Locate every uninfected red blood cell.
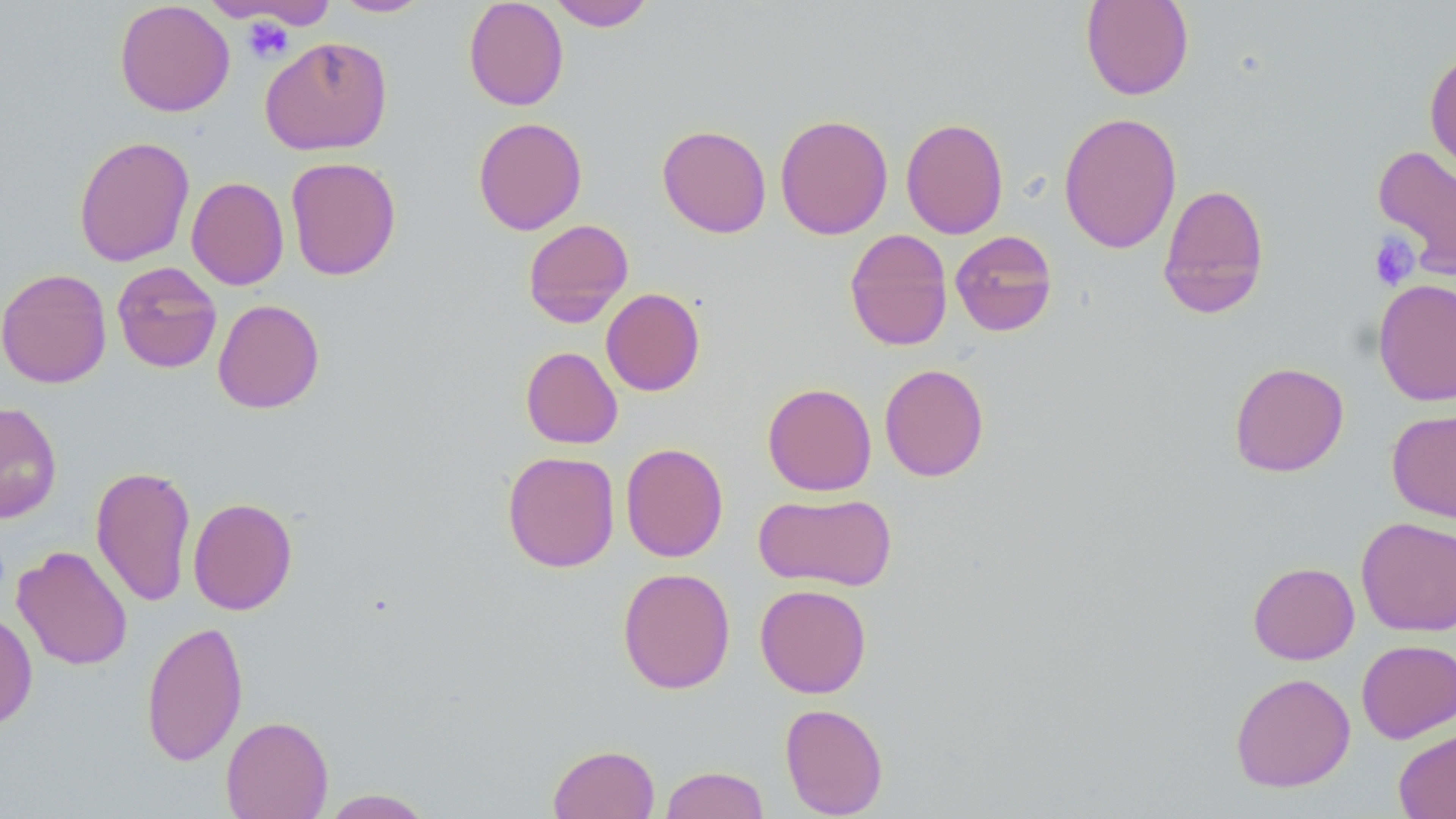

Approximate bounding boxes as (x1, y1, x2, y2) in pixels.
Uninfected red blood cells: (463, 0, 569, 111), (548, 0, 655, 31), (1080, 0, 1195, 100), (114, 1, 235, 117), (333, 1, 430, 17), (259, 36, 393, 156), (1424, 49, 1456, 178), (1058, 111, 1182, 254), (774, 113, 893, 240), (473, 116, 587, 235), (901, 117, 1008, 239), (657, 124, 772, 238), (73, 135, 195, 267), (1372, 146, 1456, 278), (285, 157, 401, 281), (186, 176, 289, 290), (1157, 183, 1271, 318), (523, 218, 634, 327), (844, 229, 953, 351), (950, 230, 1058, 337), (112, 261, 222, 373), (0, 268, 112, 388), (1373, 278, 1456, 406), (601, 288, 705, 396), (212, 299, 325, 414), (520, 346, 623, 449), (1228, 361, 1349, 477), (879, 363, 989, 482), (762, 382, 877, 496), (0, 401, 62, 524), (1386, 409, 1456, 523), (620, 442, 729, 562), (502, 451, 620, 572), (91, 464, 196, 607), (753, 491, 897, 592), (188, 497, 298, 615), (1356, 517, 1455, 636), (12, 545, 133, 671), (1247, 561, 1359, 664), (617, 567, 736, 694), (755, 584, 872, 698), (0, 610, 38, 732), (141, 619, 248, 767), (1356, 639, 1456, 743), (1230, 672, 1356, 792), (780, 702, 889, 818), (220, 715, 334, 819), (1393, 727, 1456, 818), (547, 744, 660, 819), (659, 765, 770, 819), (320, 788, 435, 818).

slide-level diagnosis = no evidence of blood parasites
magnification = 1000x
platelet locations = approximate bounding boxes as (x1, y1, x2, y2) in pixels: (241, 17, 293, 63), (1368, 232, 1420, 291)
field of view = one of a larger specimen
image size = 1456×819 pixels
stain = May-Grünwald-Giemsa
preparation = thin blood smear
modality = optical microscopy